Report the malaria status of this cell.
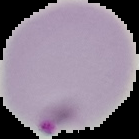
It is parasitized.

Cell region segmented out of the field of view; the surrounding area is masked to black. From a thin blood film. Image is 139×139 pixels.